Identify the cell.
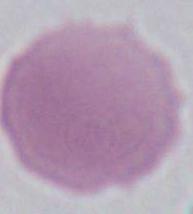

An erythrocyte.

Captured at 1000x magnification. Micrograph.